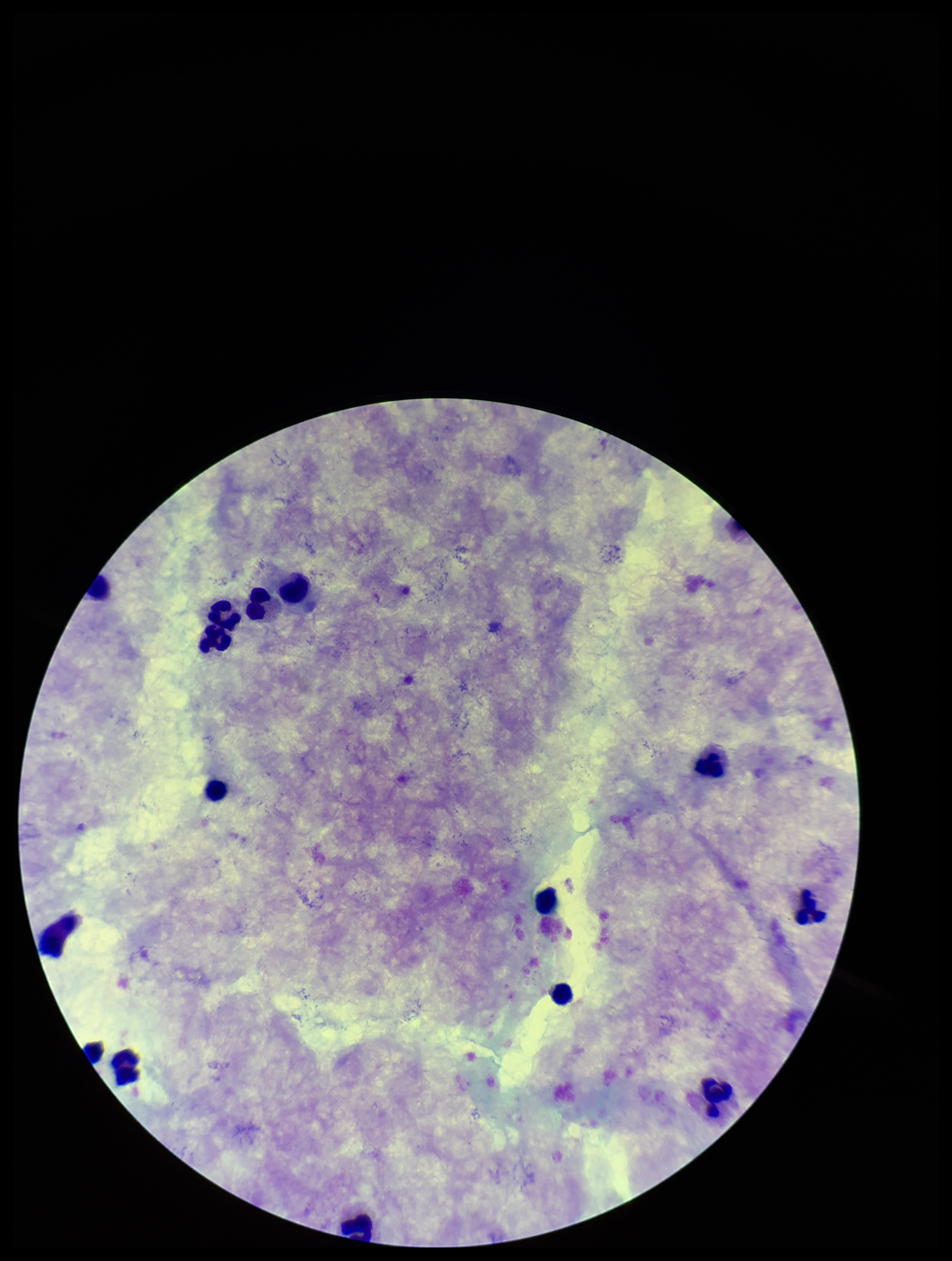

{
  "capture": "smartphone photograph through the microscope eyepiece",
  "patient_malaria_status": "negative",
  "field_of_view": "one from this slide",
  "leukocyte_count": 13,
  "parasite_count": 0,
  "preparation": "thick blood smear",
  "image_size": "952×1261 pixels",
  "stain": "Giemsa",
  "plasmodium_parasites": "none detected"
}